Report the malaria status of this cell.
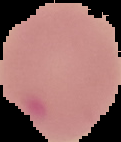

It is uninfected.

preparation = thin blood smear
image size = 121×142 pixels
image type = segmented cell region with the area outside set to black